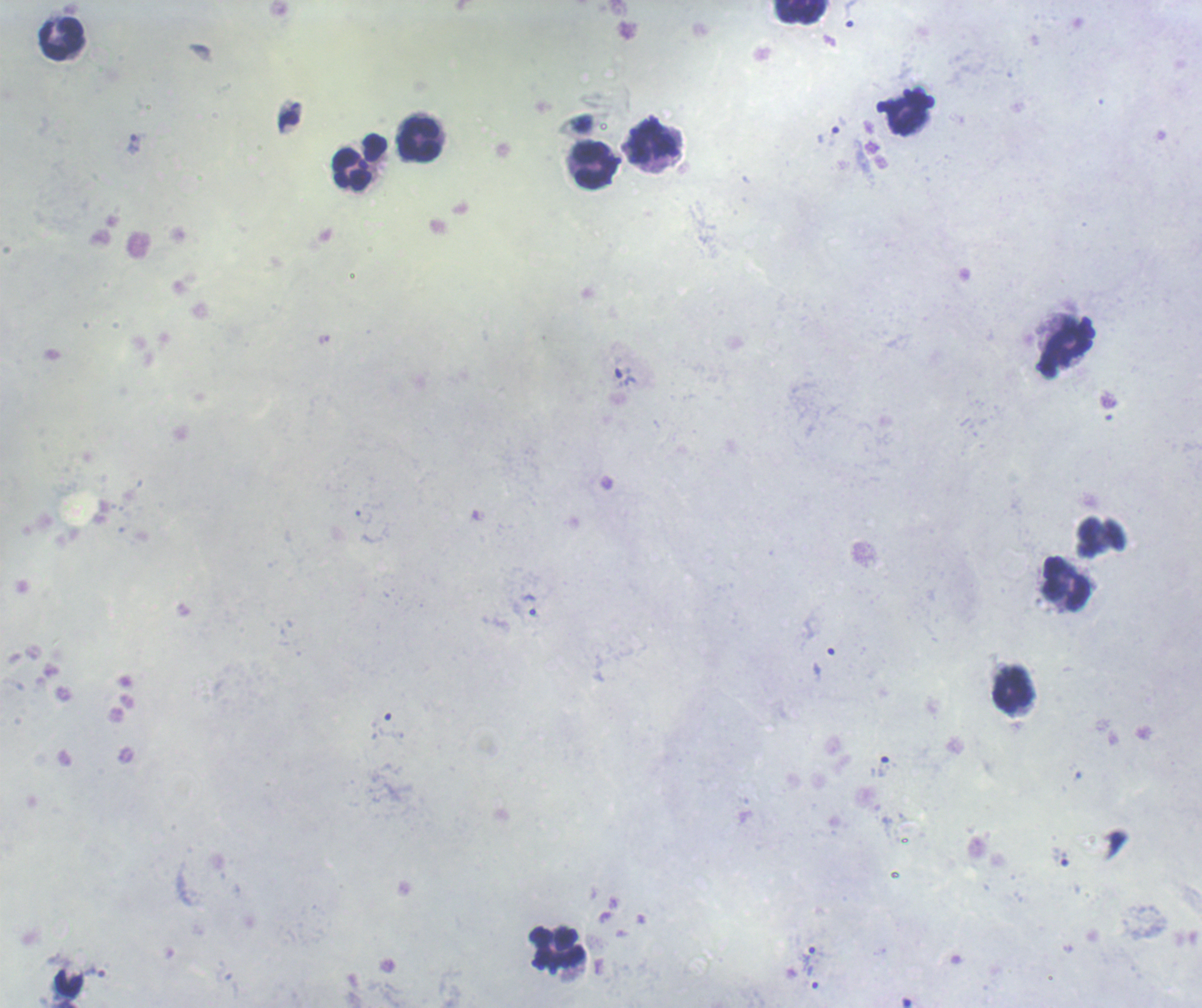

coordinate format = approximate centers as (x, y) in pixels
trophozoite locations = (850, 14), (831, 130), (134, 143), (624, 378), (530, 605), (880, 766), (1062, 858), (808, 955), (95, 973), (813, 977)
leukocyte locations = (801, 11), (62, 39), (906, 113), (420, 139), (651, 141), (359, 162), (595, 165), (1068, 347), (1066, 583), (1013, 689), (559, 947), (68, 982)
preparation = thick blood smear
result = malaria parasites identified
magnification = 100x
field of view = single
context = previously used in a real diagnosis
stain = Romanowsky
background quality = unsatisfactory
image size = 1202×1008 pixels